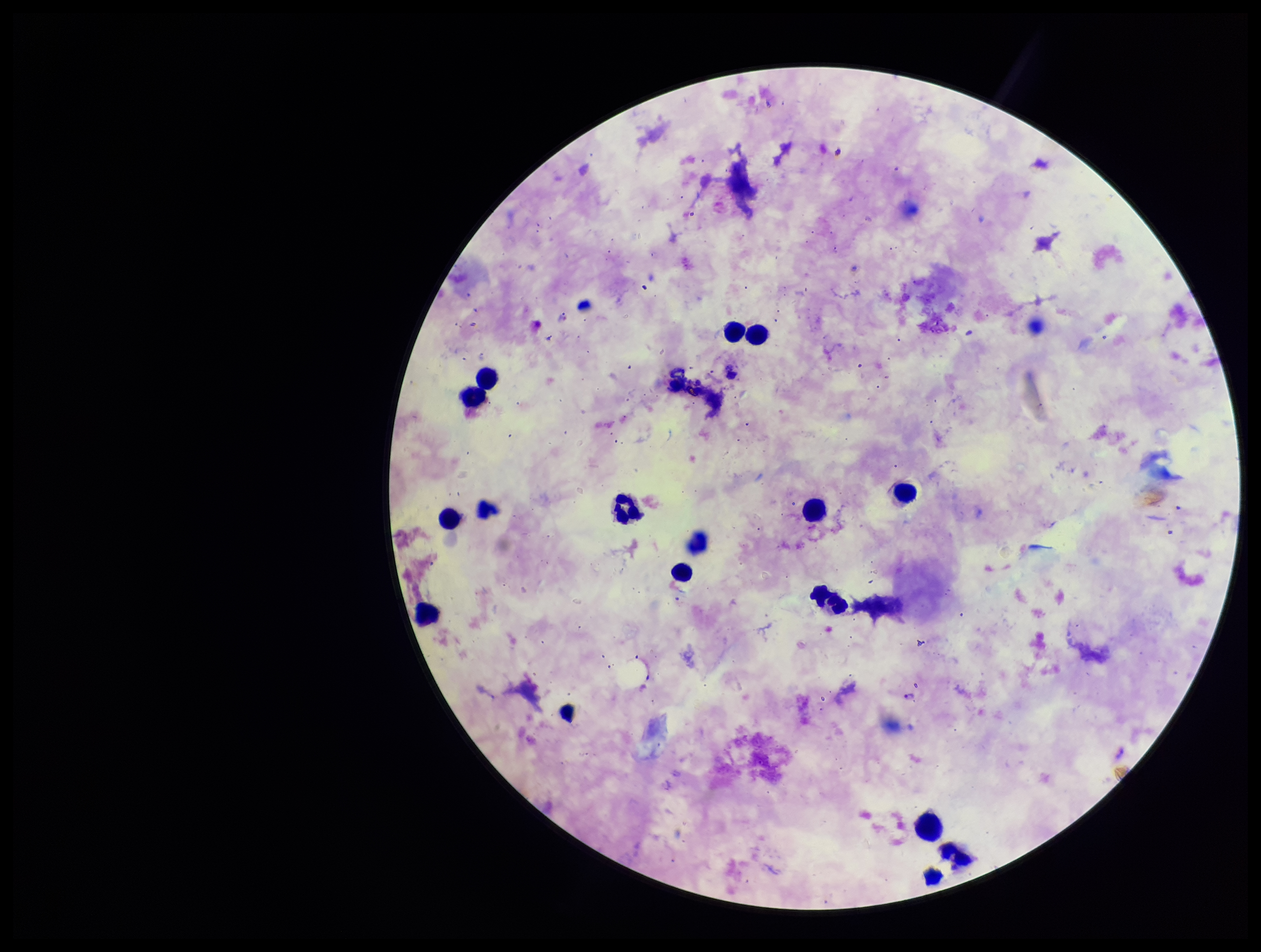
stain = Giemsa
species reported for this patient = Plasmodium falciparum
image size = 1261×952 pixels
leukocyte count = 15
parasite count = 1
capture = smartphone photograph through the microscope eyepiece
field of view = single
preparation = thick smear
patient malaria status = positive
Plasmodium parasites = detected